State which parasite is depicted.
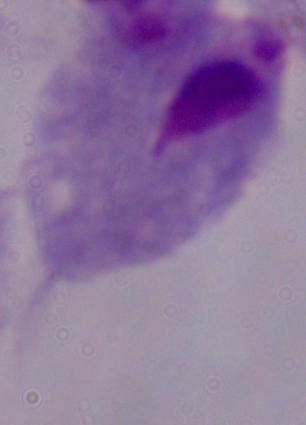
A trichomonad.

Summary:
  - Magnification: 1000x
  - Modality: micrograph